Give the position of every Plasmodium parasite.
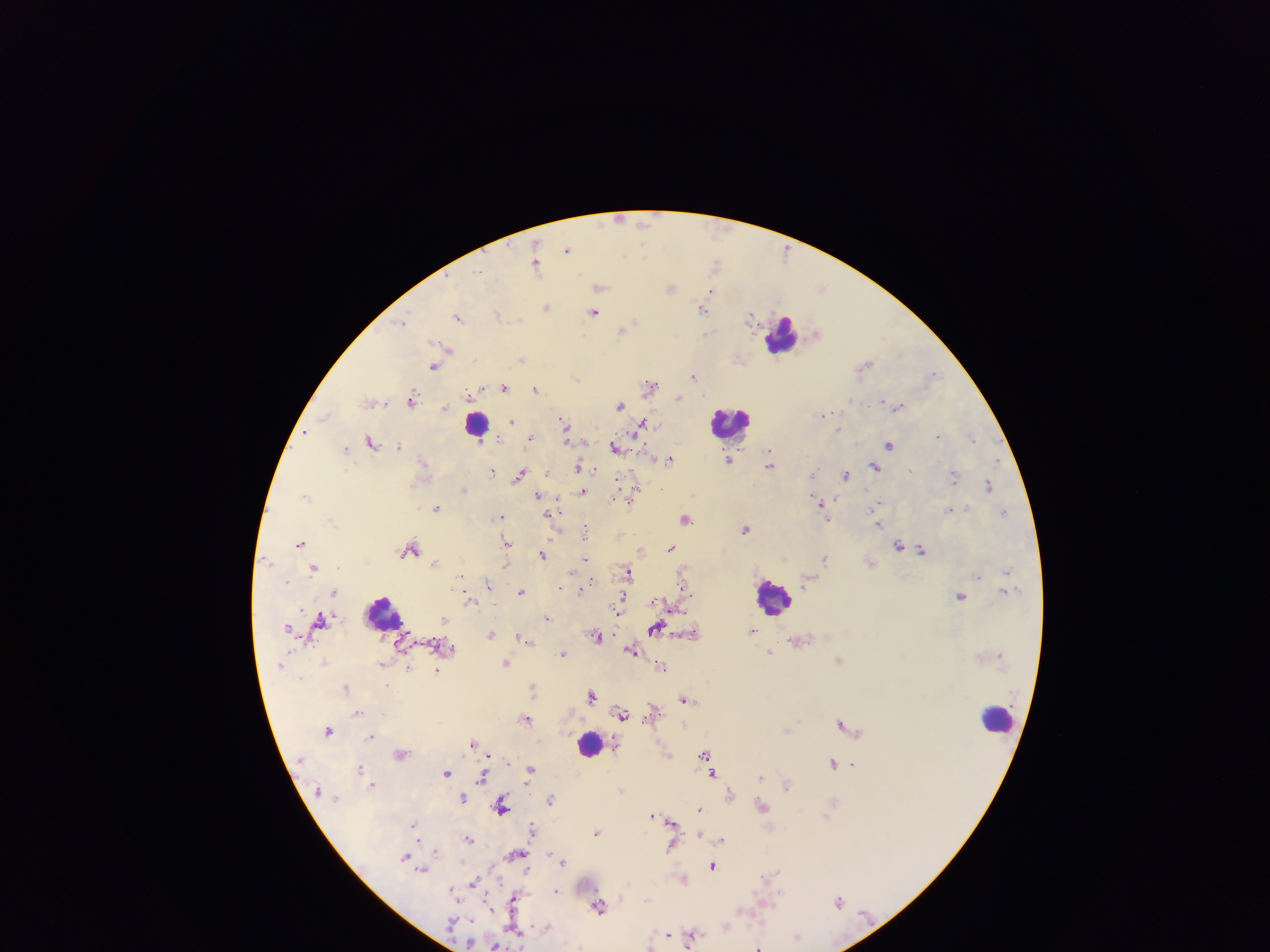
Approximate centers as x y in pixels.
Plasmodium parasites: 618 219; 645 222; 567 249; 644 250; 715 263; 537 265; 478 271; 600 286; 671 287; 822 288; 712 291; 547 306; 704 309; 594 312; 499 313; 751 315; 458 318; 404 321; 633 321; 622 329; 707 333; 816 334; 448 349; 522 358; 865 365; 434 366; 932 375; 693 376; 576 377; 650 385; 503 388; 536 389; 467 396; 679 397; 412 398; 883 401; 370 402; 620 404; 899 407; 445 408; 822 414; 325 415; 512 421; 565 425; 642 425; 839 429; 306 432; 567 435; 938 436; 532 437; 974 438; 371 441; 890 444; 399 445; 615 448; 345 449; 669 460; 729 460; 997 460; 770 463; 579 466; 874 466; 492 471; 813 472; 846 474; 519 475; 954 477; 989 485; 634 488; 465 489; 867 491; 583 492; 305 495; 538 495; 615 497; 633 497; 836 500; 878 503; 821 504; 436 508; 950 510; 1004 513; 500 516; 685 519; 827 519; 879 524; 746 528; 586 531; 508 542; 300 543; 899 545; 671 548; 411 549; 640 549; 922 550; 543 553; 825 558; 586 559; 267 560; 436 562; 314 567; 1007 571; 627 572; 978 576; 287 581; 683 582; 488 584; 561 587; 582 589; 521 591; 335 592; 961 596; 469 600; 620 603; 671 606; 618 608; 546 618; 444 620; 321 621; 287 627; 656 628; 752 631; 490 635; 595 636; 523 638; 632 650; 770 652; 563 653; 506 663; 661 666; 408 668; 437 671; 387 685; 346 687; 533 687; 592 695; 684 699; 652 710; 358 712; 623 714; 526 719; 842 724; 787 729; 328 731; 372 737; 473 743; 400 754; 704 754; 834 762; 359 768; 531 771; 446 772; 713 773; 483 777; 761 777; 787 784; 372 785; 621 789; 731 793; 463 798; 550 800; 833 802; 501 805; 762 806; 700 810; 652 815; 671 824; 414 825; 532 828; 597 832; 468 838; 721 840; 672 848; 436 851; 516 854; 405 857; 563 860; 713 866; 422 871; 771 875; 684 878; 474 883; 452 891; 556 891; 514 899; 839 901; 599 906; 725 925; 546 927; 514 930; 666 934; 692 935; 797 935; 469 944; 496 946; 758 946.

Leukocyte locations: 783 335; 477 423; 732 423; 772 597; 384 612; 997 717; 590 743. One field of view. Mobile-phone photograph taken through the microscope. Image is 1270×952 pixels. Sample from Ghana. Thick blood film.